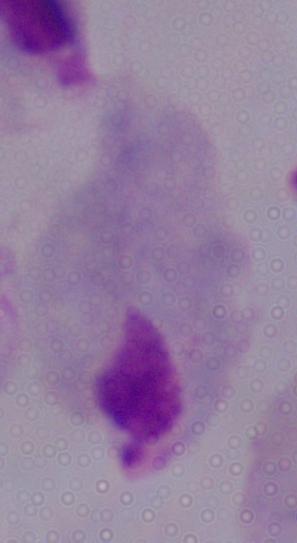 A trichomonad is seen. Micrograph. Captured at 1000x magnification.